State the blood parasite species.
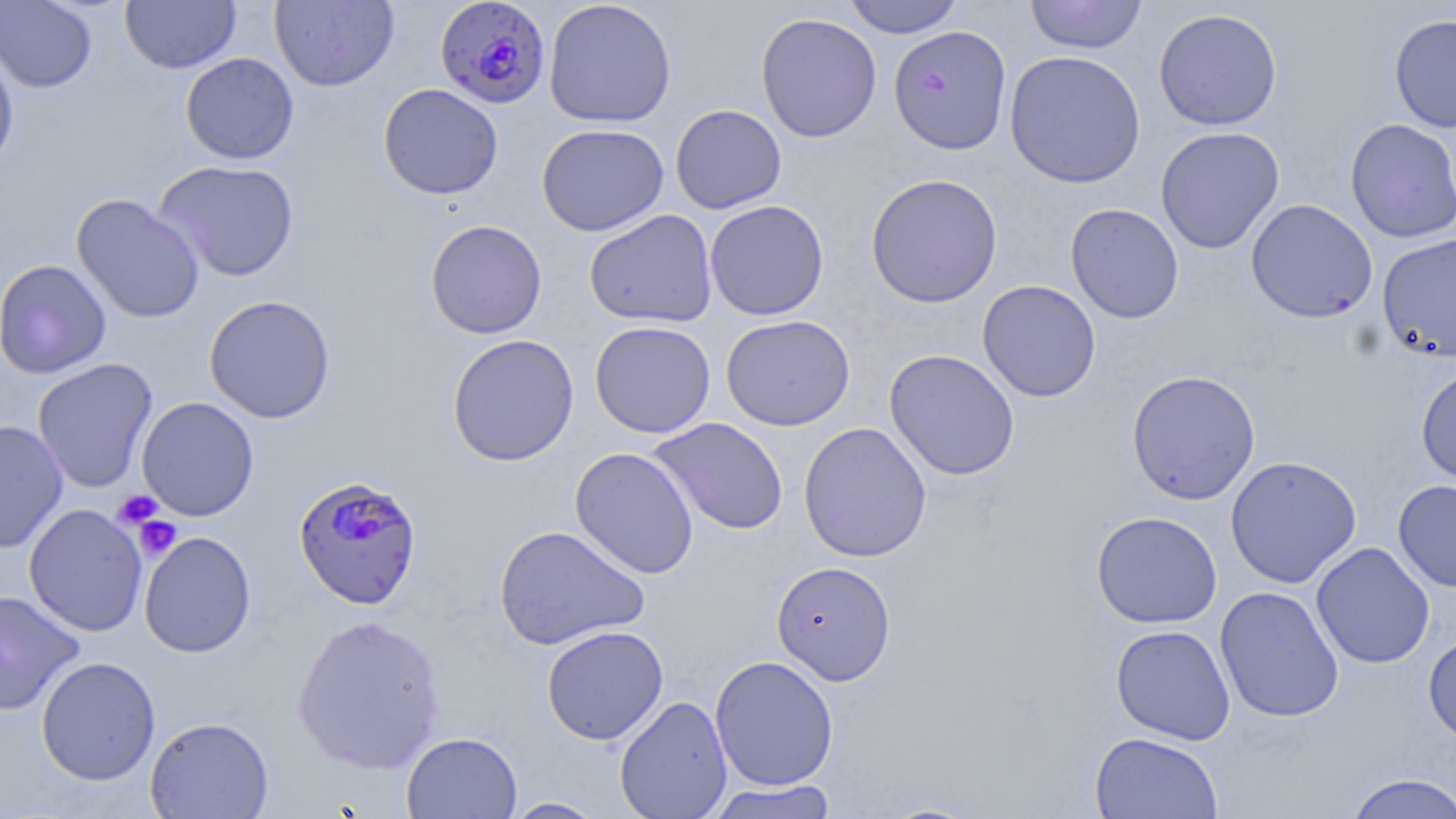
Plasmodium falciparum.

uninfected_red_blood_cell_locations: 'approximate bounding boxes as (x1,y1)-(x2,y2) corner pairs in pixels: (0,0)-(97,93), (543,0)-(676,128), (842,0)-(964,38), (1025,0)-(1147,54), (120,1)-(241,73), (270,1)-(399,91), (1154,7)-(1282,131), (755,13)-(882,143), (1388,13)-(1456,134), (888,25)-(1012,155), (0,43)-(19,176), (1004,49)-(1146,189), (180,52)-(299,164), (378,83)-(504,199), (670,104)-(787,214), (1345,118)-(1456,243), (537,123)-(669,236), (1155,126)-(1285,254), (152,159)-(300,281), (866,172)-(1003,308), (71,193)-(205,324), (1246,199)-(1378,324), (704,200)-(829,321), (1065,203)-(1184,324), (584,210)-(718,328), (426,220)-(547,339), (1376,233)-(1456,363), (0,259)-(111,379), (977,279)-(1101,402), (204,294)-(336,423), (721,314)-(855,431), (590,320)-(715,439), (446,333)-(580,467), (884,349)-(1020,480), (32,359)-(158,493), (1416,363)-(1456,488), (1126,369)-(1261,505), (136,396)-(259,521), (649,417)-(789,536), (0,419)-(68,554), (798,422)-(932,562), (570,447)-(699,579), (1225,455)-(1361,588), (1392,479)-(1456,592), (24,504)-(148,636), (1091,511)-(1222,628), (493,524)-(650,650), (138,531)-(256,657), (1311,542)-(1435,669), (771,560)-(896,686), (1214,586)-(1344,723), (0,590)-(86,715), (291,614)-(446,774), (1111,624)-(1235,744), (541,625)-(669,745), (1423,631)-(1456,745), (710,654)-(839,791), (36,656)-(161,785), (614,695)-(732,819), (144,715)-(274,818), (402,731)-(522,819), (1089,732)-(1224,819), (1343,772)-(1456,818), (704,779)-(838,819), (503,797)-(607,818)'
magnification: 1000x
plasmodium_falciparum_infected_red_blood_cell_locations: 'approximate bounding boxes as (x1,y1)-(x2,y2) corner pairs in pixels: (430,1)-(547,110), (294,477)-(425,611)'
preparation: thin blood smear
stain: May-Grünwald-Giemsa
image_size: 1456×819 pixels
field_of_view: single
modality: light microscopy
platelet_locations: 'approximate bounding boxes as (x1,y1)-(x2,y2) corner pairs in pixels: (113,490)-(163,530), (134,516)-(181,561)'